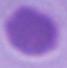
magnification: 1000x
modality: micrograph
identification: erythrocyte